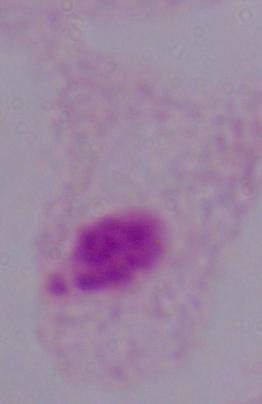
A trichomonad is seen. Photomicrograph. 1000x magnification.